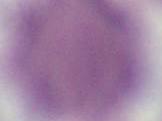

Summary:
  - Modality: micrograph
  - Identification: red blood cell
  - Magnification: 1000x